Report the malaria status of this cell.
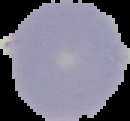
It is uninfected.

image type = cell region segmented out of the field of view; surrounding area masked to black
image size = 130×121 pixels
preparation = thin blood film